State which cell type is depicted.
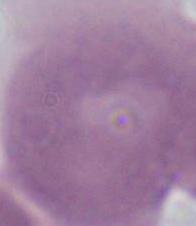

This is an erythrocyte.

Captured at 1000x magnification. Photomicrograph.